Locate every Plasmodium parasite.
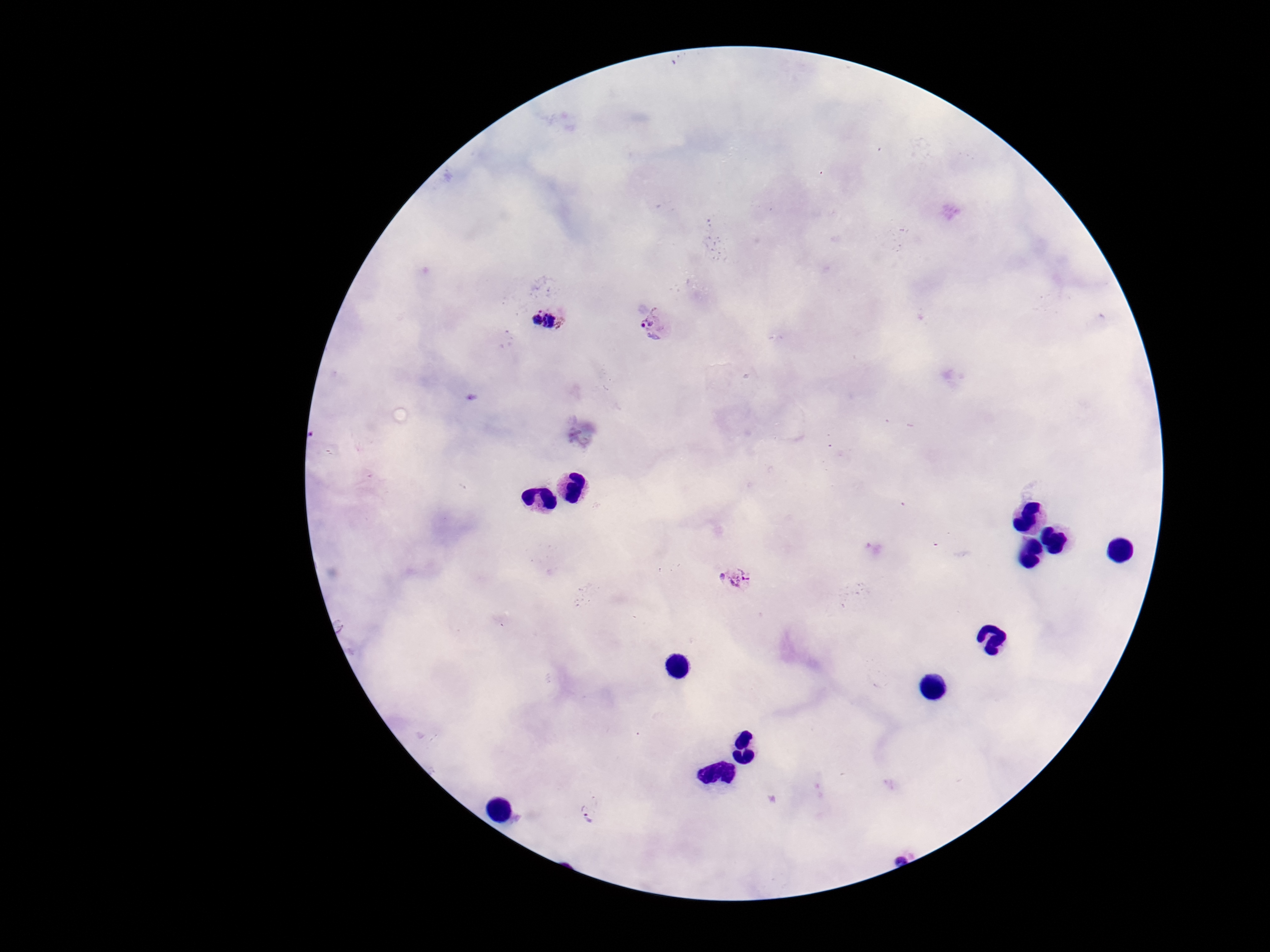
Approximate centers as {x, y} in pixels.
Plasmodium parasites: {545, 312}, {658, 324}, {740, 579}, {588, 808}.

Summary:
  - Magnification: 100x
  - Field of view: one from this slide
  - Stain: Giemsa
  - Patient malaria status: positive
  - Image size: 1270×952 pixels
  - Capture: smartphone camera through the microscope eyepiece
  - Preparation: thick blood film